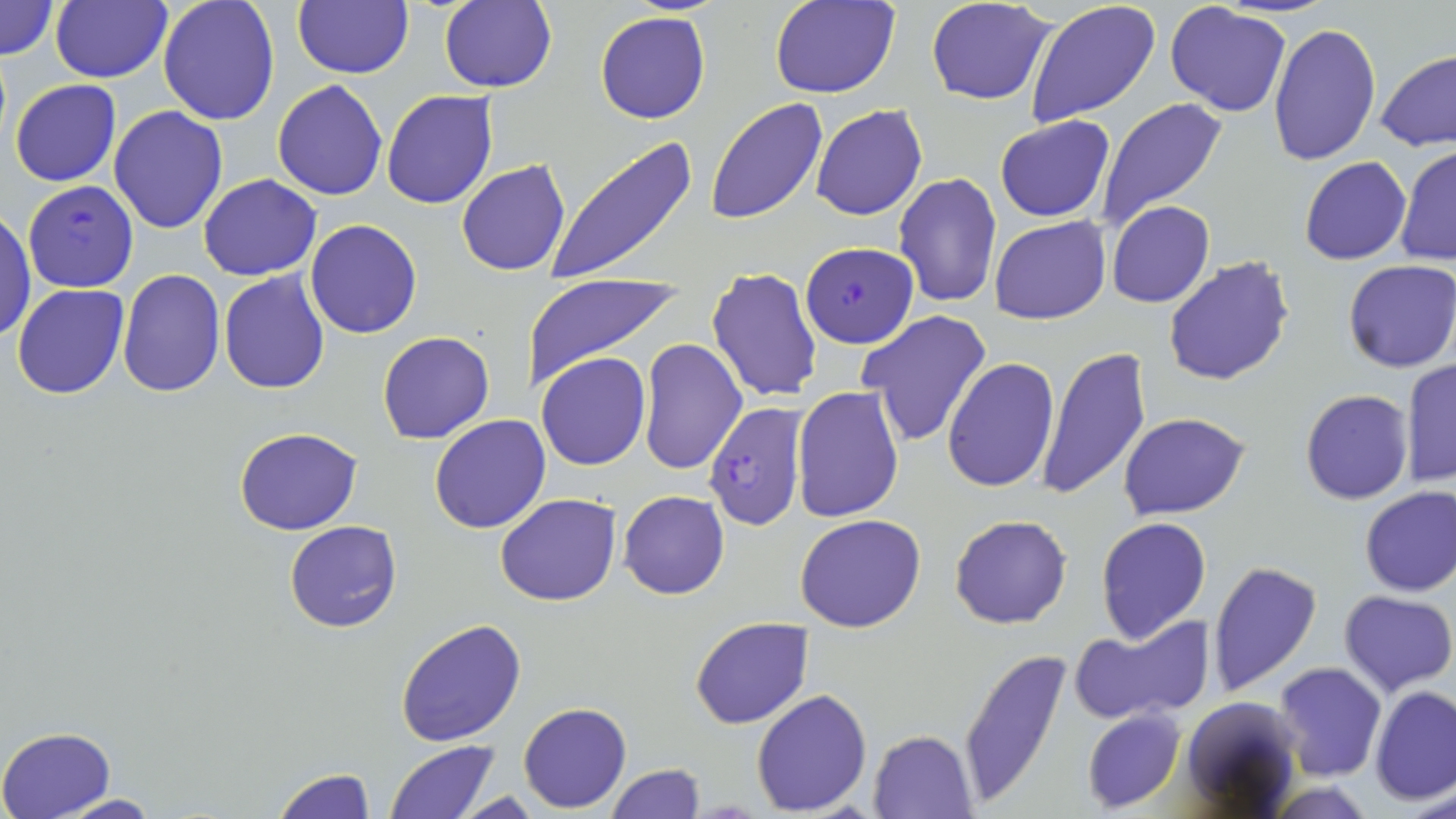 Approximate bounding boxes as (x1,y1)-(x2,y2) corner pairs in pixels. Plasmodium falciparum-infected red blood cell locations: (23,180)-(138,291), (802,243)-(917,347), (702,404)-(807,532). Uninfected red blood cell locations: (0,0)-(60,61), (50,0)-(172,84), (157,0)-(281,126), (293,0)-(413,79), (769,0)-(900,99), (925,0)-(1058,105), (1024,0)-(1162,127), (439,1)-(557,92), (1165,2)-(1291,117), (595,10)-(710,124), (1266,21)-(1382,166), (1374,49)-(1456,153), (272,79)-(387,201), (10,80)-(122,186), (381,90)-(499,210), (705,95)-(829,226), (1095,97)-(1229,232), (810,103)-(927,221), (109,107)-(229,234), (993,116)-(1116,222), (546,138)-(698,284), (1396,145)-(1455,266), (1300,156)-(1411,265), (456,160)-(572,277), (894,170)-(1003,308), (198,174)-(322,281), (1107,201)-(1215,309), (1,207)-(36,344), (989,215)-(1112,325), (304,219)-(422,339), (1163,256)-(1296,388), (1343,259)-(1456,374), (118,269)-(225,396), (705,269)-(820,405), (218,270)-(331,394), (518,271)-(685,390), (12,283)-(129,400), (855,309)-(993,449), (376,331)-(495,444), (637,338)-(747,474), (1035,345)-(1152,502), (536,352)-(651,471), (942,357)-(1061,493), (1401,358)-(1456,490), (792,386)-(904,521), (1300,389)-(1414,505), (1118,412)-(1251,521), (428,414)-(551,534), (233,426)-(364,534), (1358,487)-(1456,597), (617,490)-(730,599), (494,494)-(621,606), (795,513)-(927,633), (949,514)-(1073,629), (1094,516)-(1211,643), (283,521)-(404,632), (1207,561)-(1324,697), (1337,590)-(1455,696), (690,615)-(814,729), (1069,616)-(1216,726), (395,618)-(527,748), (956,646)-(1072,805), (1273,661)-(1387,781), (1370,686)-(1455,806), (751,688)-(873,813), (1178,694)-(1305,815), (518,701)-(632,813), (1081,709)-(1185,812), (0,726)-(116,818), (868,729)-(979,818), (383,739)-(504,819), (606,764)-(705,819), (272,766)-(378,819), (1264,781)-(1378,817), (54,792)-(164,818), (451,793)-(547,817). Slide-level diagnosis: Plasmodium falciparum. Thin blood smear. Image is 1456×819 pixels. Light microscopy. May-Grünwald-Giemsa stain. Captured at 1000x magnification. One field of a larger specimen.